Name the parasite shown.
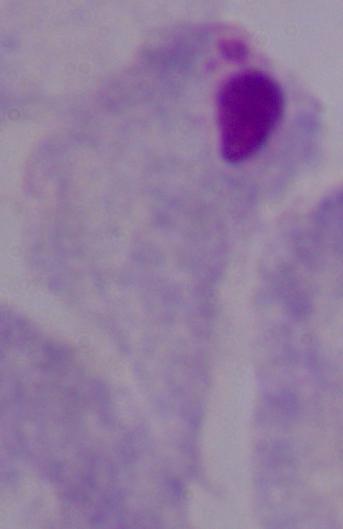

This is a trichomonad.

Captured at 1000x magnification. Micrograph.